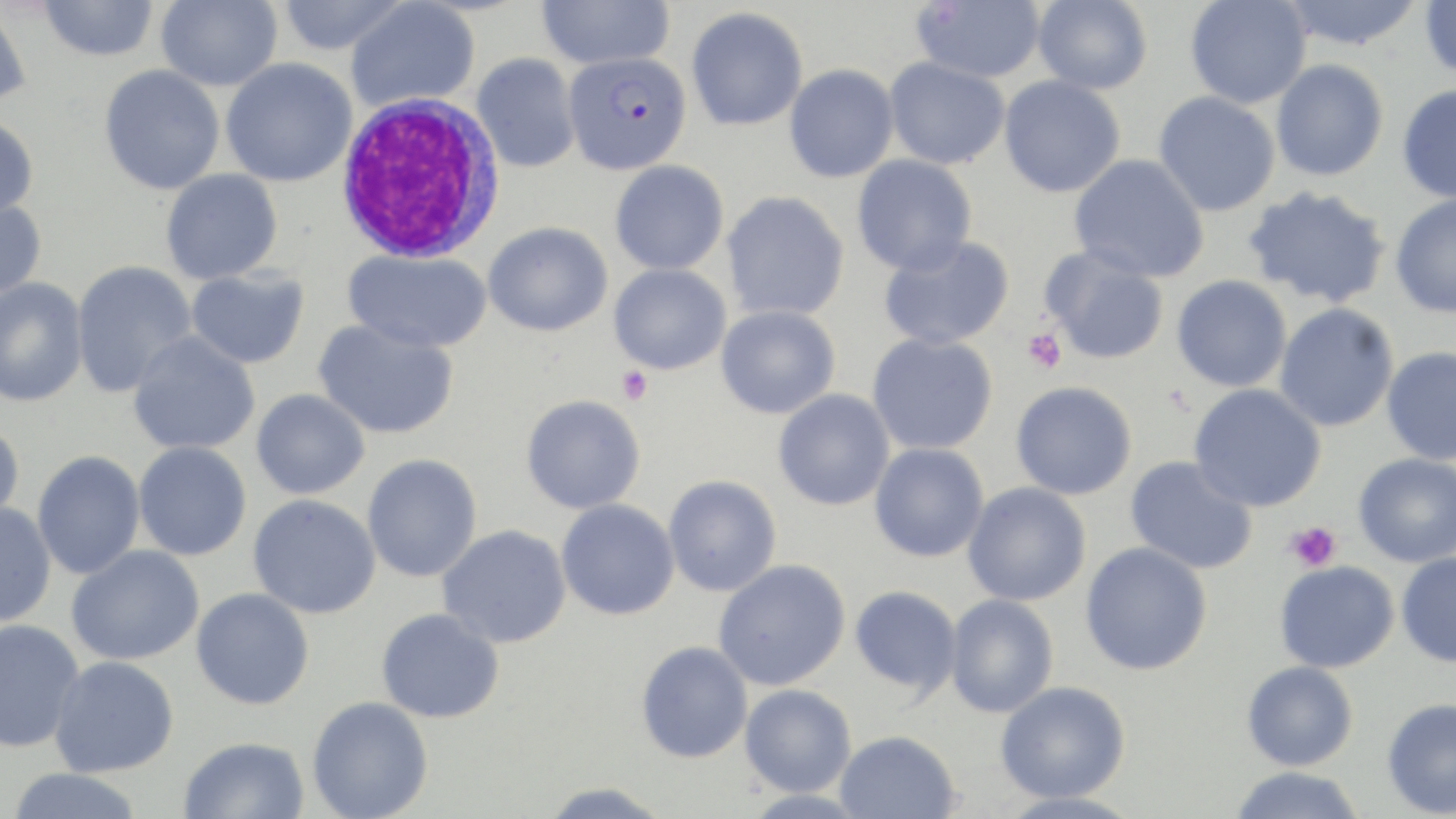
Approximate bounding boxes as named x1/y1/x2/y2 corners in pixels. Uninfected red blood cell locations: (x1=38, y1=0, x2=159, y2=62), (x1=155, y1=0, x2=283, y2=92), (x1=276, y1=0, x2=410, y2=56), (x1=536, y1=0, x2=675, y2=70), (x1=913, y1=0, x2=1045, y2=83), (x1=1033, y1=0, x2=1153, y2=95), (x1=1279, y1=0, x2=1424, y2=51), (x1=1419, y1=0, x2=1456, y2=79), (x1=345, y1=1, x2=480, y2=112), (x1=1185, y1=1, x2=1312, y2=109), (x1=0, y1=3, x2=32, y2=110), (x1=686, y1=7, x2=808, y2=131), (x1=472, y1=53, x2=581, y2=173), (x1=884, y1=56, x2=1010, y2=170), (x1=220, y1=58, x2=357, y2=187), (x1=1271, y1=59, x2=1388, y2=181), (x1=784, y1=64, x2=899, y2=183), (x1=98, y1=65, x2=225, y2=195), (x1=999, y1=75, x2=1125, y2=198), (x1=1397, y1=84, x2=1456, y2=203), (x1=1153, y1=91, x2=1281, y2=217), (x1=0, y1=115, x2=39, y2=221), (x1=852, y1=154, x2=977, y2=275), (x1=1069, y1=154, x2=1210, y2=282), (x1=610, y1=160, x2=729, y2=275), (x1=160, y1=169, x2=283, y2=284), (x1=1242, y1=185, x2=1392, y2=308), (x1=722, y1=191, x2=849, y2=321), (x1=1390, y1=193, x2=1456, y2=318), (x1=0, y1=198, x2=47, y2=301), (x1=483, y1=221, x2=613, y2=337), (x1=878, y1=234, x2=1014, y2=351), (x1=1039, y1=244, x2=1169, y2=365), (x1=343, y1=249, x2=491, y2=353), (x1=71, y1=260, x2=197, y2=397), (x1=609, y1=263, x2=730, y2=375), (x1=187, y1=268, x2=310, y2=369), (x1=1172, y1=275, x2=1292, y2=392), (x1=0, y1=278, x2=88, y2=407), (x1=1274, y1=303, x2=1399, y2=432), (x1=716, y1=305, x2=841, y2=419), (x1=313, y1=318, x2=458, y2=439), (x1=127, y1=332, x2=260, y2=455), (x1=867, y1=332, x2=998, y2=455), (x1=1381, y1=346, x2=1456, y2=465), (x1=1011, y1=381, x2=1137, y2=500), (x1=1189, y1=383, x2=1327, y2=512), (x1=251, y1=389, x2=369, y2=500), (x1=772, y1=389, x2=895, y2=511), (x1=521, y1=395, x2=645, y2=514), (x1=0, y1=420, x2=25, y2=529), (x1=133, y1=441, x2=252, y2=561), (x1=870, y1=443, x2=989, y2=562), (x1=32, y1=451, x2=145, y2=580), (x1=1353, y1=453, x2=1456, y2=568), (x1=362, y1=454, x2=483, y2=583), (x1=1125, y1=456, x2=1258, y2=575), (x1=663, y1=475, x2=781, y2=597), (x1=963, y1=482, x2=1091, y2=606), (x1=248, y1=494, x2=382, y2=619), (x1=555, y1=498, x2=680, y2=620), (x1=0, y1=502, x2=56, y2=627), (x1=437, y1=524, x2=571, y2=648), (x1=1080, y1=542, x2=1213, y2=675), (x1=65, y1=545, x2=204, y2=666), (x1=1396, y1=552, x2=1456, y2=667), (x1=713, y1=559, x2=850, y2=691), (x1=1275, y1=561, x2=1399, y2=672), (x1=850, y1=585, x2=961, y2=695), (x1=191, y1=587, x2=314, y2=710), (x1=945, y1=593, x2=1059, y2=719), (x1=376, y1=607, x2=505, y2=723), (x1=0, y1=619, x2=84, y2=752), (x1=636, y1=640, x2=753, y2=763), (x1=49, y1=655, x2=180, y2=777), (x1=1242, y1=661, x2=1358, y2=771), (x1=995, y1=680, x2=1130, y2=803), (x1=739, y1=683, x2=856, y2=797), (x1=307, y1=696, x2=433, y2=819), (x1=1381, y1=697, x2=1456, y2=817), (x1=835, y1=730, x2=961, y2=818), (x1=178, y1=736, x2=310, y2=819), (x1=1229, y1=766, x2=1365, y2=819), (x1=5, y1=768, x2=146, y2=819), (x1=540, y1=782, x2=674, y2=818), (x1=998, y1=791, x2=1143, y2=819). Plasmodium falciparum-infected red blood cell locations: (x1=563, y1=51, x2=692, y2=175). Platelet locations: (x1=1022, y1=327, x2=1067, y2=374), (x1=616, y1=366, x2=654, y2=405), (x1=1285, y1=522, x2=1341, y2=571). White blood cell locations: (x1=334, y1=93, x2=505, y2=263). Slide-level diagnosis: Plasmodium falciparum. Thin blood smear. Optical microscopy. One field of a larger specimen. 1000x magnification. Image is 1456×819 pixels. May-Grünwald-Giemsa-stained preparation.